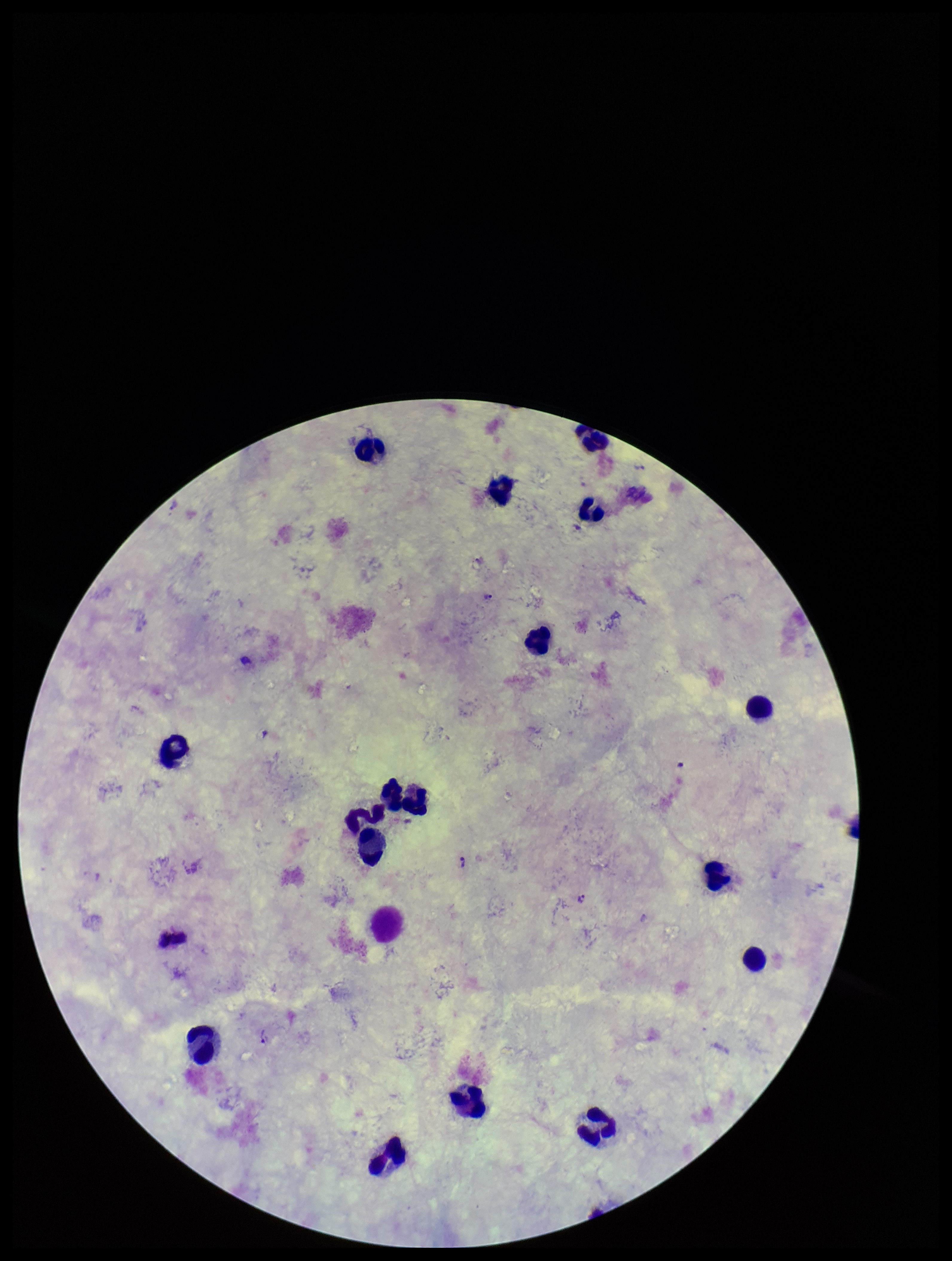
Summary:
  - Parasite count: 4
  - Field of view: one from this slide
  - Leukocyte count: 16
  - Capture: smartphone photograph through the microscope eyepiece
  - Stain: Giemsa
  - Image size: 952×1261 pixels
  - Preparation: thick blood smear
  - Patient malaria status: positive
  - Plasmodium parasites: detected
  - Species reported for this patient: Plasmodium vivax